Point out each leukocyte.
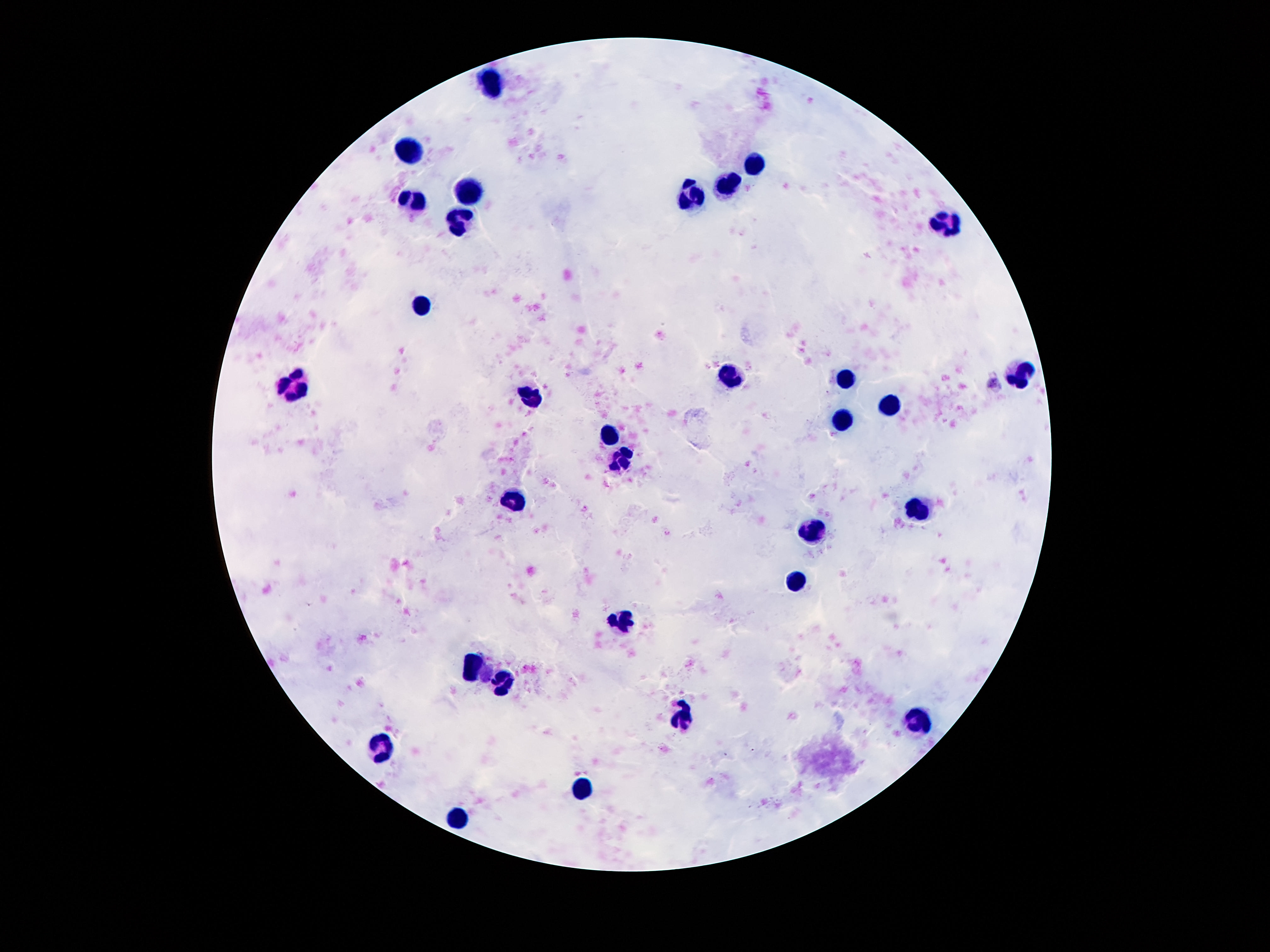
Approximate centers as {x, y} in pixels.
Leukocytes: {491, 81}, {410, 149}, {758, 161}, {729, 186}, {468, 193}, {693, 195}, {410, 200}, {945, 222}, {458, 223}, {420, 305}, {1021, 370}, {731, 377}, {846, 378}, {292, 388}, {531, 399}, {892, 403}, {840, 420}, {609, 437}, {619, 462}, {508, 501}, {918, 509}, {815, 534}, {796, 579}, {622, 623}, {473, 667}, {498, 682}, {680, 716}, {915, 720}, {382, 750}, {580, 787}, {456, 817}.

{
  "preparation": "thick peripheral-blood smear",
  "patient_malaria_status": "not infected",
  "image_size": "1270×952 pixels",
  "capture": "smartphone camera through the microscope eyepiece",
  "stain": "Giemsa",
  "magnification": "100x",
  "field_of_view": "one from this slide"
}